Assess this cell for malaria.
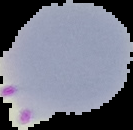
Parasitized.

Image is 133×130 pixels. The area outside the segmented cell region is set to black. From a thin blood film.